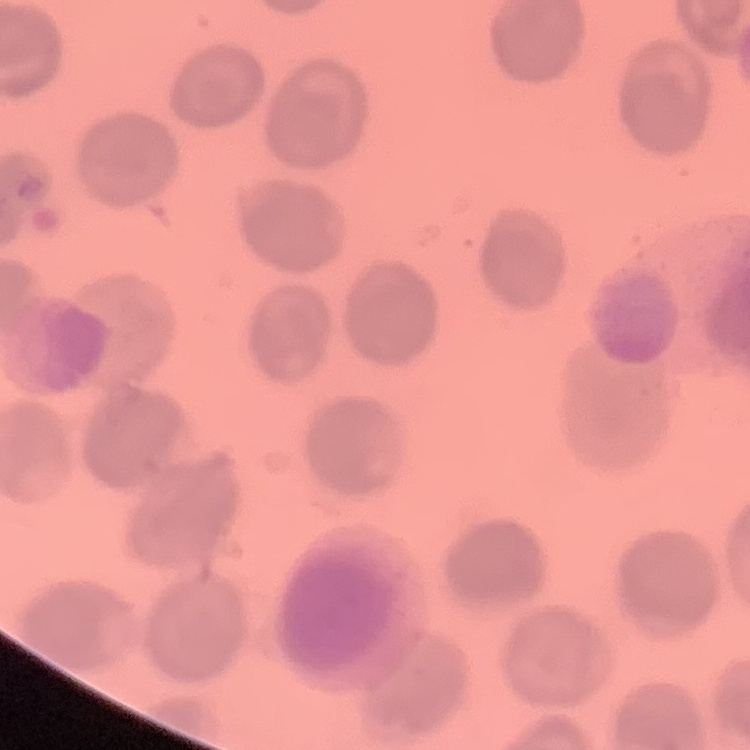
The red blood cells exhibit no rouleaux formation. Thin peripheral smear. One tile cut from a larger photomicrograph. Stained with either Field's or Giemsa.